Assess this cell for malaria.
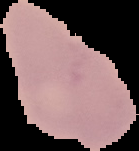
It is uninfected.

Summary:
  - Image type: cell region segmented out of the field of view; surrounding area masked to black
  - Preparation: thin blood film
  - Image size: 139×151 pixels